Identify the cell.
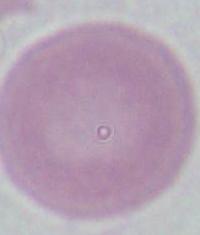

This is an erythrocyte.

modality = photomicrograph
magnification = 1000x